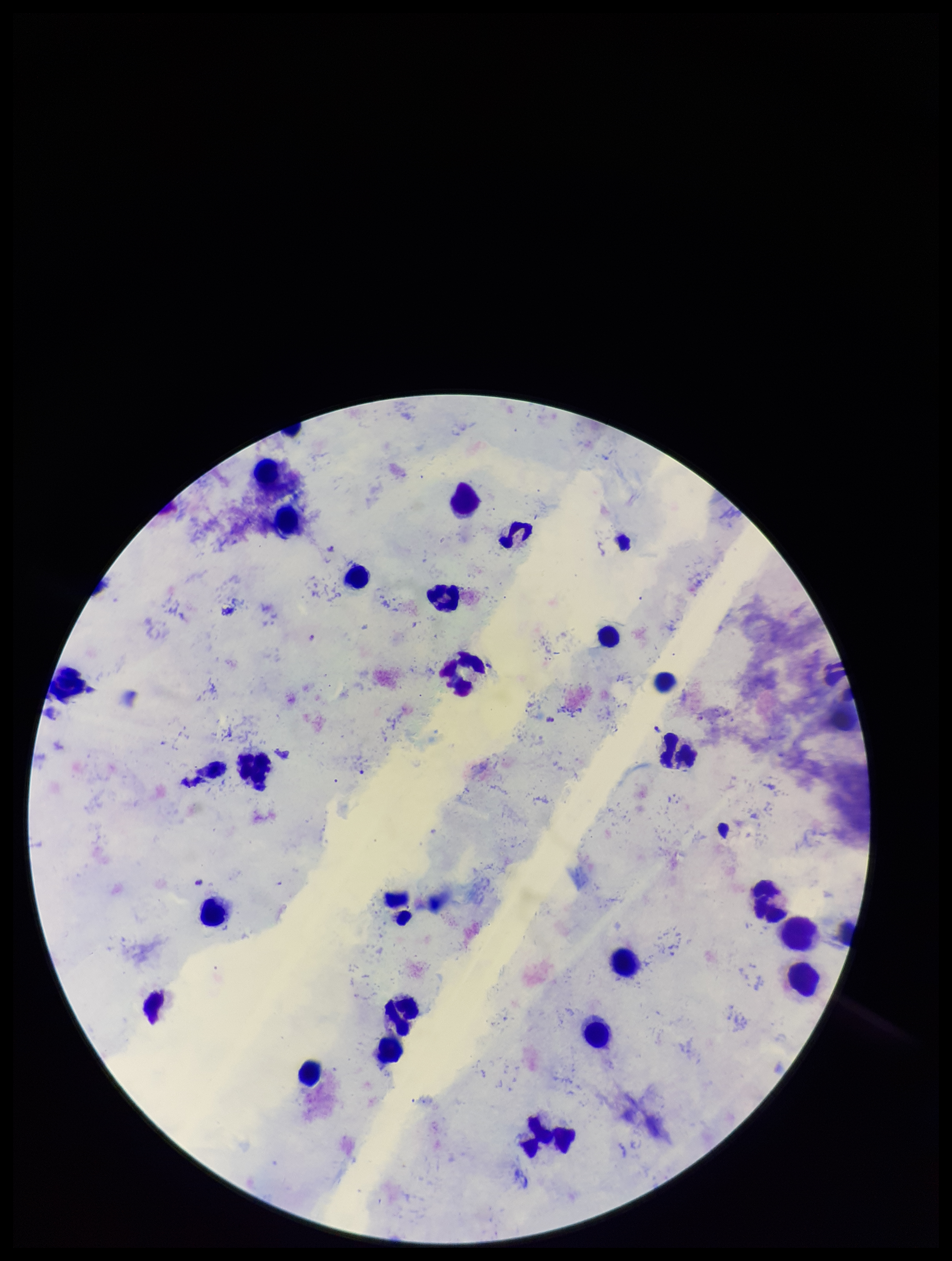 Photographed through the microscope eyepiece with a smartphone camera. Image is 952×1261 pixels. Species reported for this patient: Plasmodium falciparum. Parasite count: 3. Single field of view. Plasmodium parasites: identified. Giemsa stain. Patient malaria status: positive. Leukocyte count: 27. Preparation: thick smear.